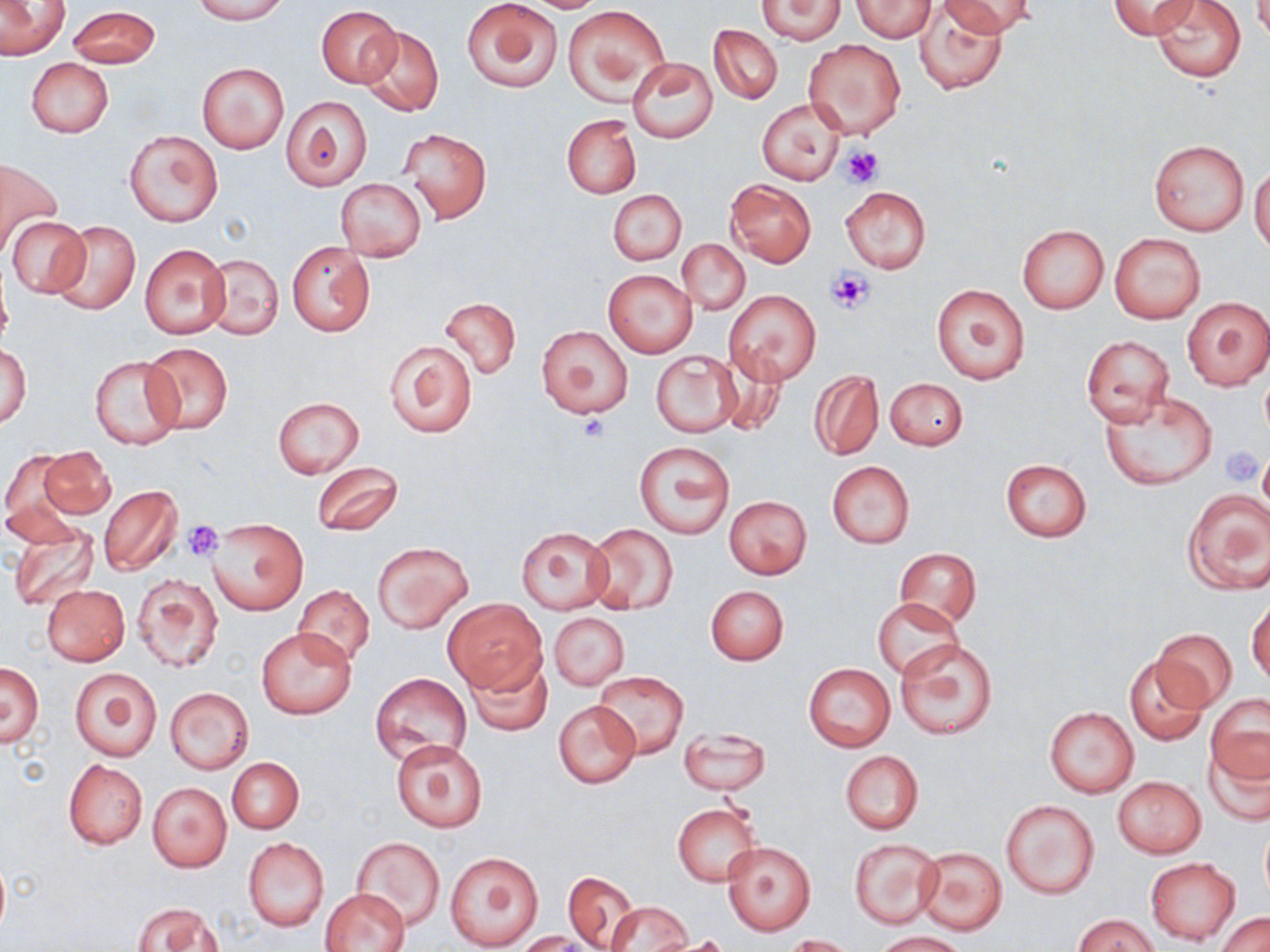
Approximate bounding boxes as (x1, y1, x2, y2) in pixels. Uninfected red blood cell locations: (0, 0, 70, 61), (192, 0, 288, 24), (462, 0, 564, 93), (520, 0, 609, 12), (758, 0, 844, 44), (852, 0, 935, 40), (913, 0, 1008, 94), (940, 0, 1038, 38), (1109, 0, 1200, 39), (1151, 0, 1246, 82), (67, 5, 161, 68), (317, 5, 402, 87), (564, 5, 667, 103), (709, 24, 782, 103), (356, 25, 444, 118), (802, 39, 906, 141), (628, 57, 718, 143), (26, 58, 114, 138), (196, 61, 290, 153), (281, 95, 373, 189), (756, 97, 846, 185), (562, 114, 641, 199), (401, 129, 490, 224), (125, 130, 223, 227), (1150, 140, 1250, 236), (1, 160, 62, 253), (1250, 164, 1270, 254), (725, 178, 815, 267), (336, 179, 426, 261), (840, 185, 931, 274), (608, 189, 685, 265), (5, 216, 91, 298), (50, 220, 141, 316), (1017, 224, 1109, 314), (1109, 232, 1206, 324), (678, 239, 749, 315), (287, 242, 375, 335), (139, 244, 230, 338), (201, 253, 283, 340), (604, 270, 697, 357), (931, 283, 1029, 385), (724, 289, 820, 385), (442, 297, 520, 378), (1182, 297, 1270, 391), (536, 324, 632, 419), (1081, 335, 1175, 425), (384, 339, 477, 438), (1, 340, 31, 431), (141, 342, 233, 434), (716, 350, 788, 436), (652, 351, 741, 437), (91, 354, 184, 449), (809, 369, 883, 459), (885, 377, 968, 450), (1100, 393, 1217, 490), (273, 397, 364, 479), (635, 441, 734, 540), (35, 445, 115, 521), (2, 452, 82, 544), (1000, 459, 1092, 542), (311, 460, 404, 538), (827, 462, 915, 548), (98, 485, 182, 576), (1182, 489, 1270, 594), (724, 496, 811, 579), (208, 518, 307, 615), (8, 521, 102, 613), (585, 524, 679, 615), (516, 527, 614, 613), (372, 541, 473, 633), (896, 548, 980, 628), (132, 573, 223, 673), (41, 585, 130, 666), (706, 585, 789, 665), (294, 586, 374, 667), (1248, 596, 1269, 686), (444, 598, 546, 693), (873, 598, 962, 678), (549, 612, 629, 690), (256, 626, 356, 719), (1153, 628, 1237, 710), (895, 640, 997, 740), (463, 652, 553, 739), (1124, 655, 1209, 745), (803, 662, 896, 752), (1, 663, 43, 746), (69, 667, 161, 761), (594, 671, 689, 758), (370, 672, 471, 765), (165, 688, 253, 772), (1207, 694, 1269, 782), (554, 700, 641, 787), (1044, 706, 1138, 797), (677, 728, 770, 795), (1204, 739, 1270, 825), (391, 740, 486, 832), (840, 751, 924, 834), (227, 757, 303, 833), (63, 759, 148, 850), (1113, 776, 1206, 858), (148, 783, 231, 872), (1002, 799, 1099, 899), (672, 802, 760, 887), (1260, 826, 1270, 902), (351, 836, 444, 930), (849, 837, 942, 928), (243, 838, 328, 931), (723, 842, 815, 934), (915, 847, 1007, 936), (445, 850, 544, 950), (0, 854, 9, 943), (1146, 857, 1241, 945), (561, 870, 641, 952), (322, 888, 410, 952), (606, 901, 691, 952), (133, 902, 225, 952), (1217, 912, 1270, 952), (1075, 913, 1159, 952), (876, 931, 969, 952), (519, 932, 591, 952), (786, 934, 856, 952), (651, 936, 733, 952). Platelet locations: (839, 144, 884, 188), (828, 268, 875, 313), (578, 414, 608, 440), (1219, 445, 1267, 483), (180, 520, 225, 562). Slide-level diagnosis: no evidence of blood parasites. Light microscopy. 1000x magnification. Thin blood smear. May-Grünwald-Giemsa stain. Single field of view. Image is 1270×952 pixels.